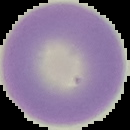
Summary:
  - Image type: segmented cell region with the area outside set to black
  - Image size: 130×130 pixels
  - Result: negative for Plasmodium parasites
  - Preparation: thin blood smear